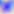

{
  "magnification": "400x",
  "modality": "photomicrograph",
  "identification": "Toxoplasma gondii"
}